Assess the morphology of the erythrocytes.
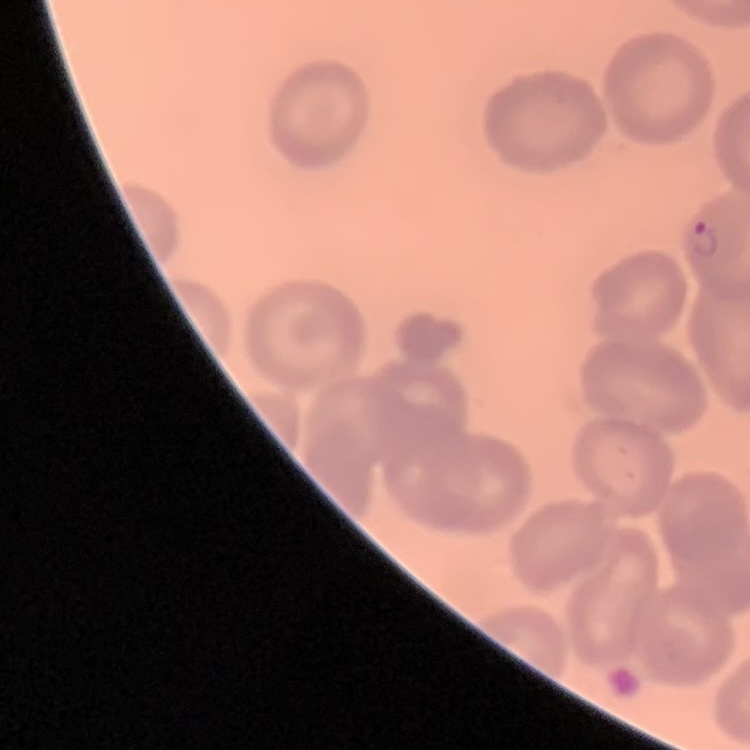
They show no rouleaux formation.

Field's or Giemsa stain. Square crop of a larger photomicrograph. Thin blood film.